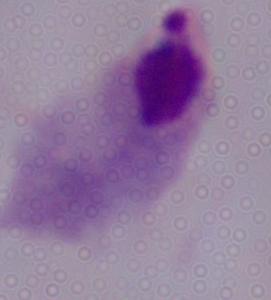
Micrograph. A trichomonad is seen. Captured at 1000x magnification.